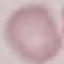
Result: no malaria parasites detected. Giemsa stain. Cell patch, automatically extracted from a larger field of view and resized to 64 × 64 pixels. Thin smear of blood. Acquired by smartphone through the microscope eyepiece.